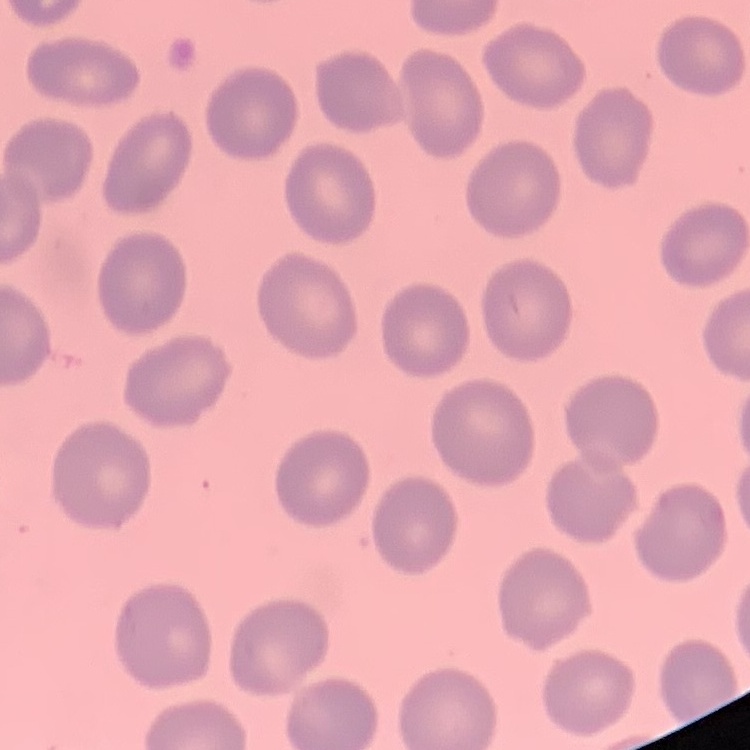

red blood cell morphology = no rouleaux formation
preparation = thin peripheral smear
stain = Field's or Giemsa
image type = square crop of a larger photomicrograph